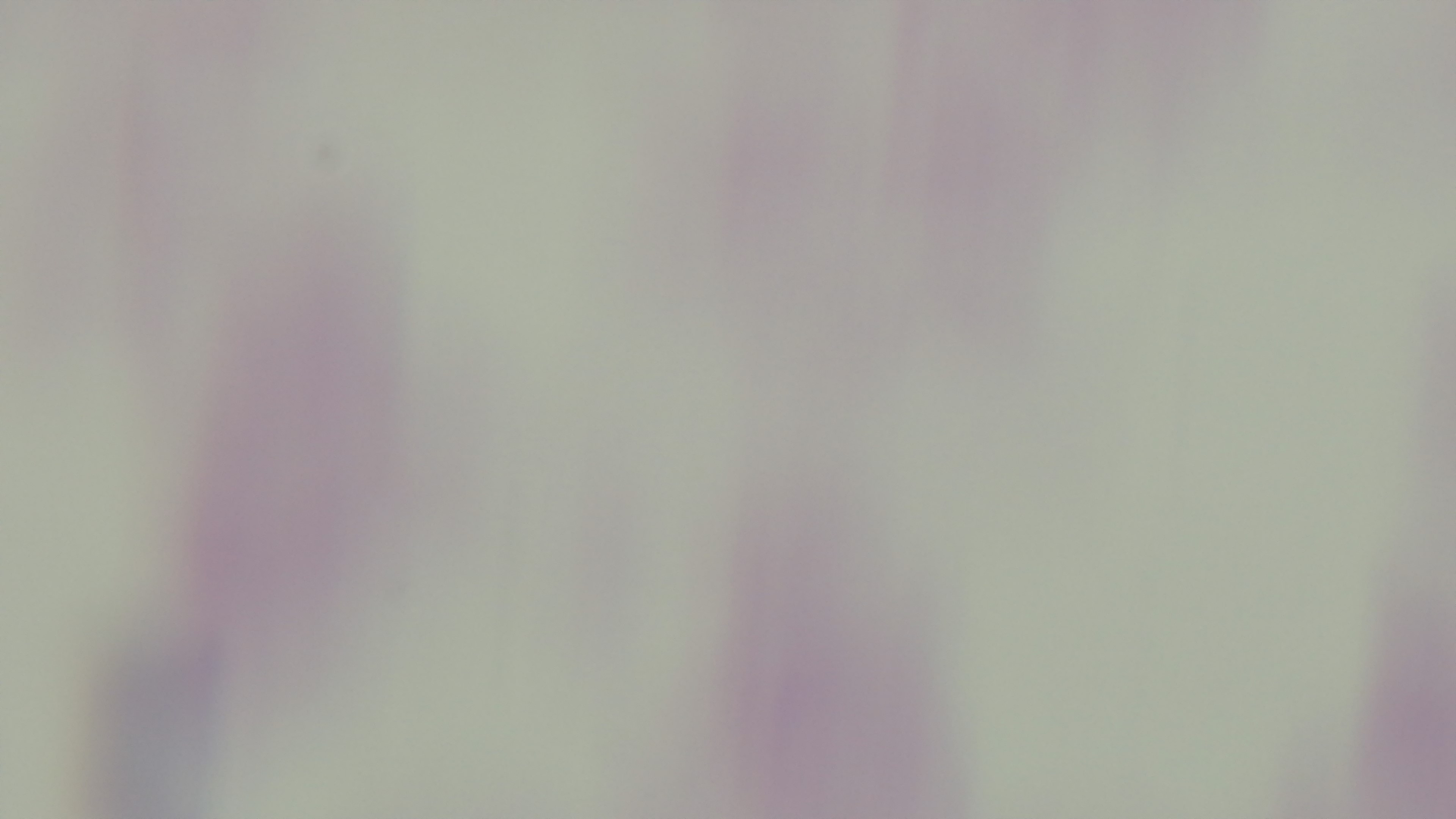

stain = Giemsa
field of view = one from the slide
modality = light microscopy
malaria status = uninfected
objective = 100x oil immersion
preparation = thick blood film
capture = mounted 4K digital camera